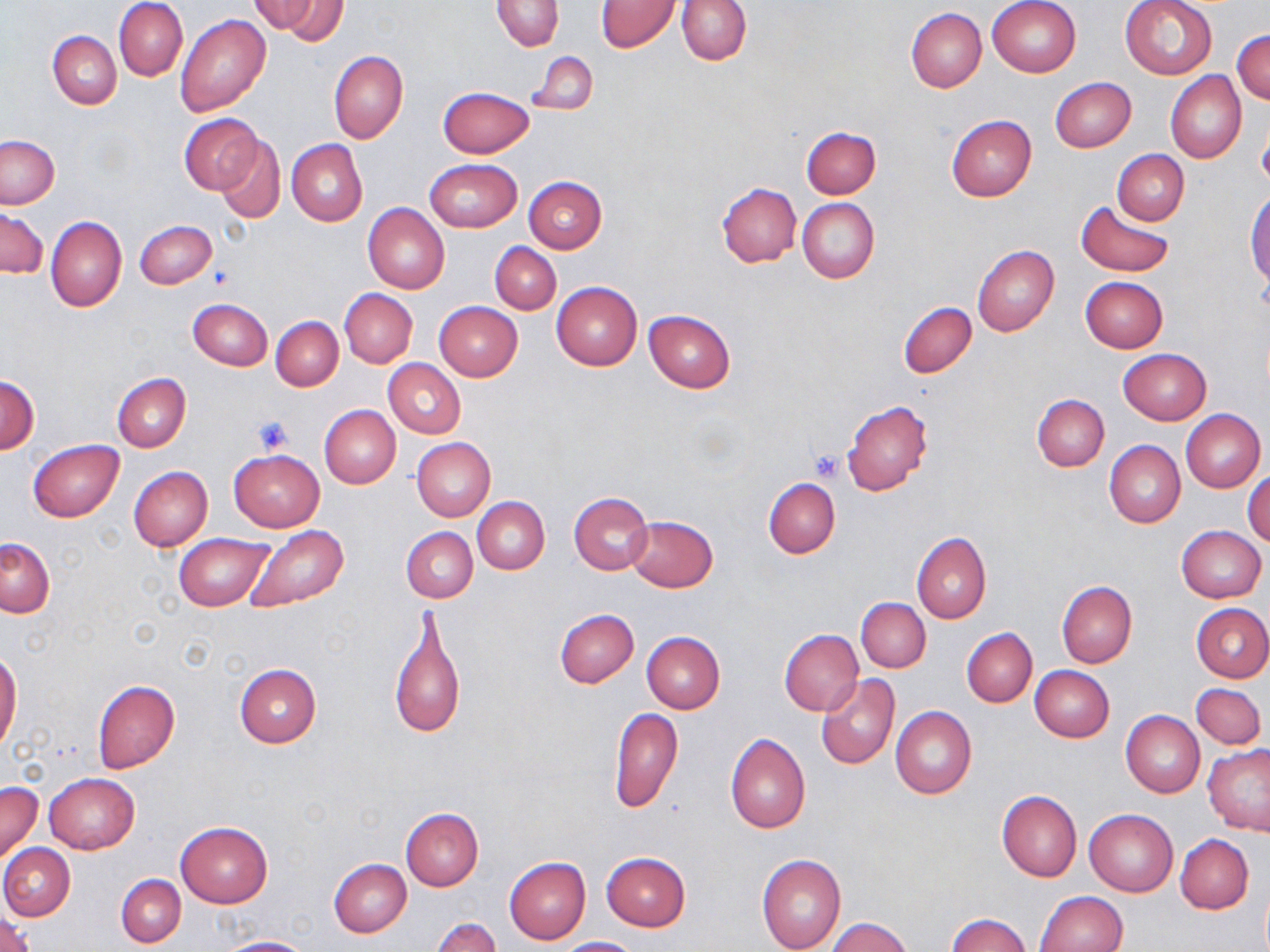 Approximate bounding boxes as (x1,y1)-(x2,y2) corner pairs in pixels. Platelet locations: (252,415)-(295,455), (809,451)-(845,480). Uninfected red blood cell locations: (115,0)-(188,81), (267,0)-(349,42), (677,0)-(750,64), (987,0)-(1082,77), (1120,0)-(1218,80), (251,1)-(320,34), (492,1)-(564,52), (596,1)-(678,52), (906,8)-(987,93), (176,14)-(271,117), (1233,28)-(1270,105), (48,30)-(121,109), (329,50)-(408,143), (529,52)-(597,116), (1165,71)-(1246,163), (1050,78)-(1135,153), (439,86)-(534,158), (180,114)-(263,195), (946,115)-(1037,201), (1258,116)-(1270,192), (802,126)-(881,198), (1,135)-(59,208), (215,137)-(285,225), (287,139)-(367,226), (1113,150)-(1188,224), (425,158)-(522,232), (523,176)-(608,253), (716,183)-(800,267), (1246,191)-(1270,289), (797,198)-(880,284), (1076,198)-(1176,278), (363,203)-(450,294), (1,208)-(47,279), (46,215)-(127,313), (135,219)-(217,289), (490,243)-(561,314), (973,244)-(1059,336), (1080,276)-(1168,352), (551,281)-(642,370), (339,289)-(417,368), (188,299)-(272,371), (898,301)-(976,378), (435,302)-(523,381), (644,310)-(736,393), (271,316)-(343,390), (1118,348)-(1211,424), (384,359)-(465,438), (113,373)-(191,453), (0,376)-(40,453), (1033,395)-(1109,471), (843,399)-(933,495), (319,405)-(400,488), (1180,408)-(1266,493), (412,438)-(496,520), (29,439)-(124,522), (1104,440)-(1185,528), (229,449)-(324,531), (128,466)-(213,550), (1245,469)-(1270,546), (764,477)-(840,558), (569,492)-(653,575), (472,497)-(549,574), (626,515)-(718,591), (1175,525)-(1267,603), (243,526)-(351,612), (402,527)-(477,603), (911,532)-(991,624), (175,533)-(272,610), (1,537)-(55,618), (1057,581)-(1137,667), (857,597)-(930,673), (1192,602)-(1270,682), (388,607)-(467,742), (555,608)-(638,688), (962,628)-(1037,706), (779,629)-(863,717), (641,631)-(725,712), (0,650)-(21,754), (234,663)-(322,747), (1030,665)-(1114,742), (815,674)-(900,771), (93,680)-(179,773), (1191,682)-(1265,751), (609,706)-(684,812), (890,707)-(976,799), (1122,711)-(1205,797), (725,733)-(810,833), (1203,744)-(1270,836), (43,773)-(140,854), (0,780)-(43,867), (996,790)-(1082,882), (400,809)-(483,890), (1085,809)-(1177,896), (176,821)-(272,908), (1176,835)-(1254,914), (0,843)-(75,920), (601,852)-(691,931), (757,854)-(845,952), (504,857)-(591,945), (329,858)-(412,937), (116,874)-(186,947), (1035,891)-(1126,952), (945,913)-(1031,951), (0,914)-(34,952), (825,917)-(913,951), (433,918)-(501,952), (216,936)-(311,952), (557,936)-(642,951). Slide-level diagnosis: no evidence of blood parasites. One field of a larger specimen. May-Grünwald-Giemsa-stained preparation. Image is 1270×952 pixels. Optical microscopy. 1000x magnification. Thin blood film.